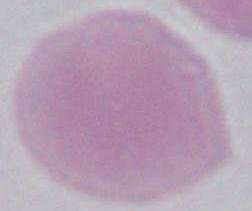 Captured at 1000x magnification. Photomicrograph. An erythrocyte is seen.